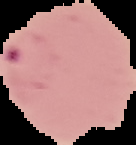
Summary:
  - Preparation: thin blood smear
  - Result: Plasmodium parasites identified
  - Image size: 136×145 pixels
  - Image type: segmented cell region on a black background